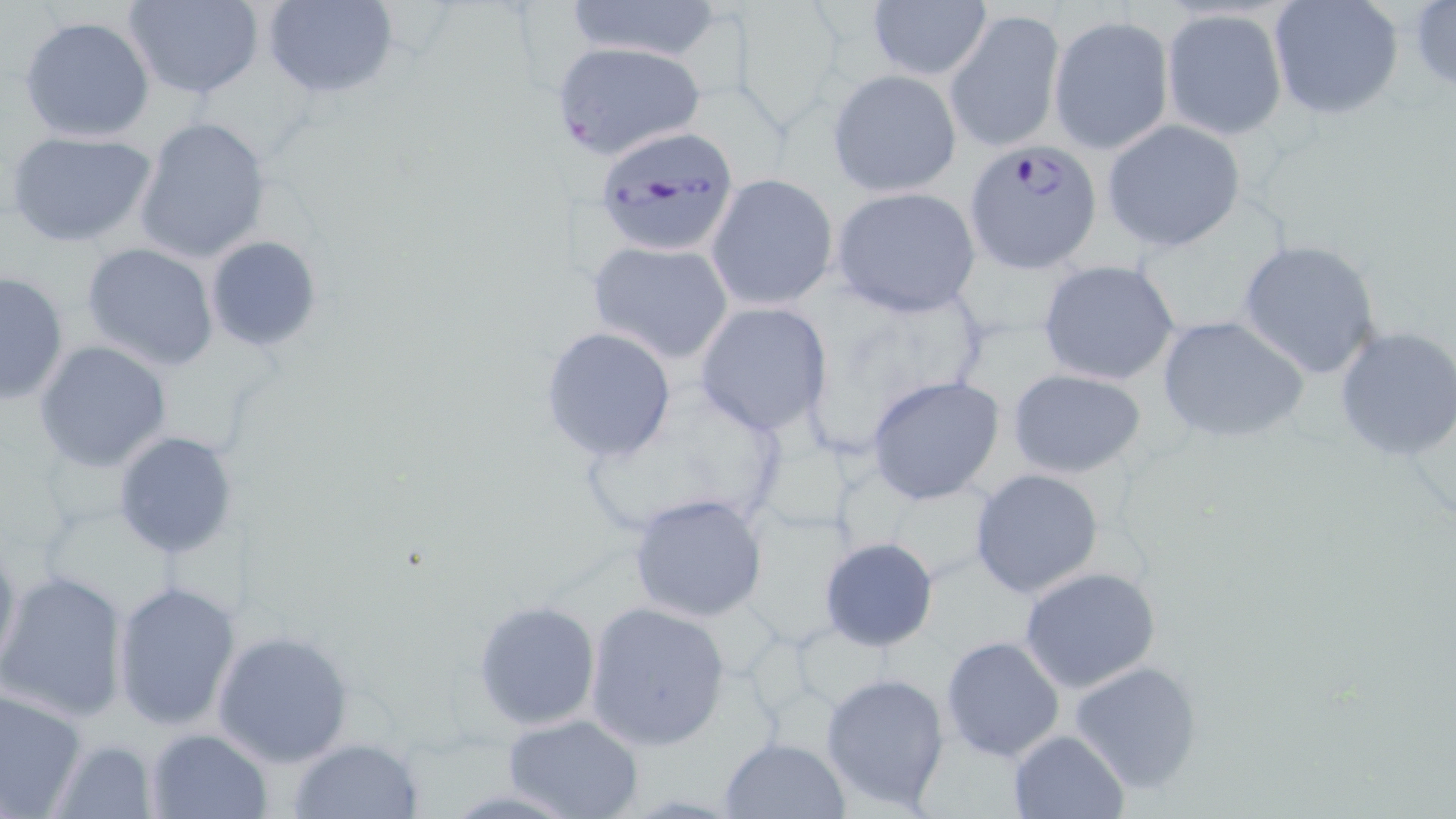
slide-level diagnosis = Plasmodium falciparum
preparation = thin blood smear
Plasmodium falciparum-infected red blood cell locations = approximate bounding boxes as (x1, y1, x2, y2) in pixels: (554, 41, 711, 160), (593, 125, 740, 256), (963, 139, 1100, 273)
field of view = one of a larger specimen
image size = 1456×819 pixels
magnification = 1000x
stain = May-Grünwald-Giemsa
modality = optical microscopy
uninfected red blood cell locations = approximate bounding boxes as (x1, y1, x2, y2) in pixels: (126, 0, 264, 99), (560, 0, 727, 64), (1268, 0, 1403, 121), (260, 1, 401, 101), (1410, 1, 1456, 93), (866, 2, 993, 83), (729, 3, 853, 127), (946, 8, 1064, 154), (1161, 8, 1288, 140), (18, 14, 157, 142), (1049, 14, 1174, 155), (829, 70, 962, 197), (134, 117, 271, 264), (1101, 118, 1246, 252), (3, 129, 159, 249), (705, 174, 839, 311), (830, 186, 984, 318), (203, 234, 324, 353), (1238, 238, 1385, 379), (588, 239, 734, 363), (80, 241, 221, 371), (1038, 259, 1183, 387), (0, 269, 70, 404), (691, 301, 835, 435), (1155, 313, 1310, 444), (537, 326, 679, 462), (1333, 326, 1456, 463), (34, 341, 172, 471), (1006, 367, 1146, 478), (573, 373, 793, 540), (867, 375, 1005, 503), (113, 431, 240, 560), (970, 468, 1105, 599), (627, 492, 771, 623), (0, 531, 21, 686), (818, 536, 940, 652), (1017, 566, 1161, 694), (0, 568, 130, 724), (111, 579, 242, 731), (471, 600, 601, 731), (584, 600, 731, 752), (212, 630, 354, 767), (940, 635, 1066, 762), (1069, 659, 1205, 793), (819, 671, 952, 811), (0, 684, 88, 819), (501, 713, 645, 819), (145, 728, 272, 818), (1007, 729, 1129, 819), (718, 736, 850, 818), (45, 737, 161, 819), (288, 737, 422, 818)